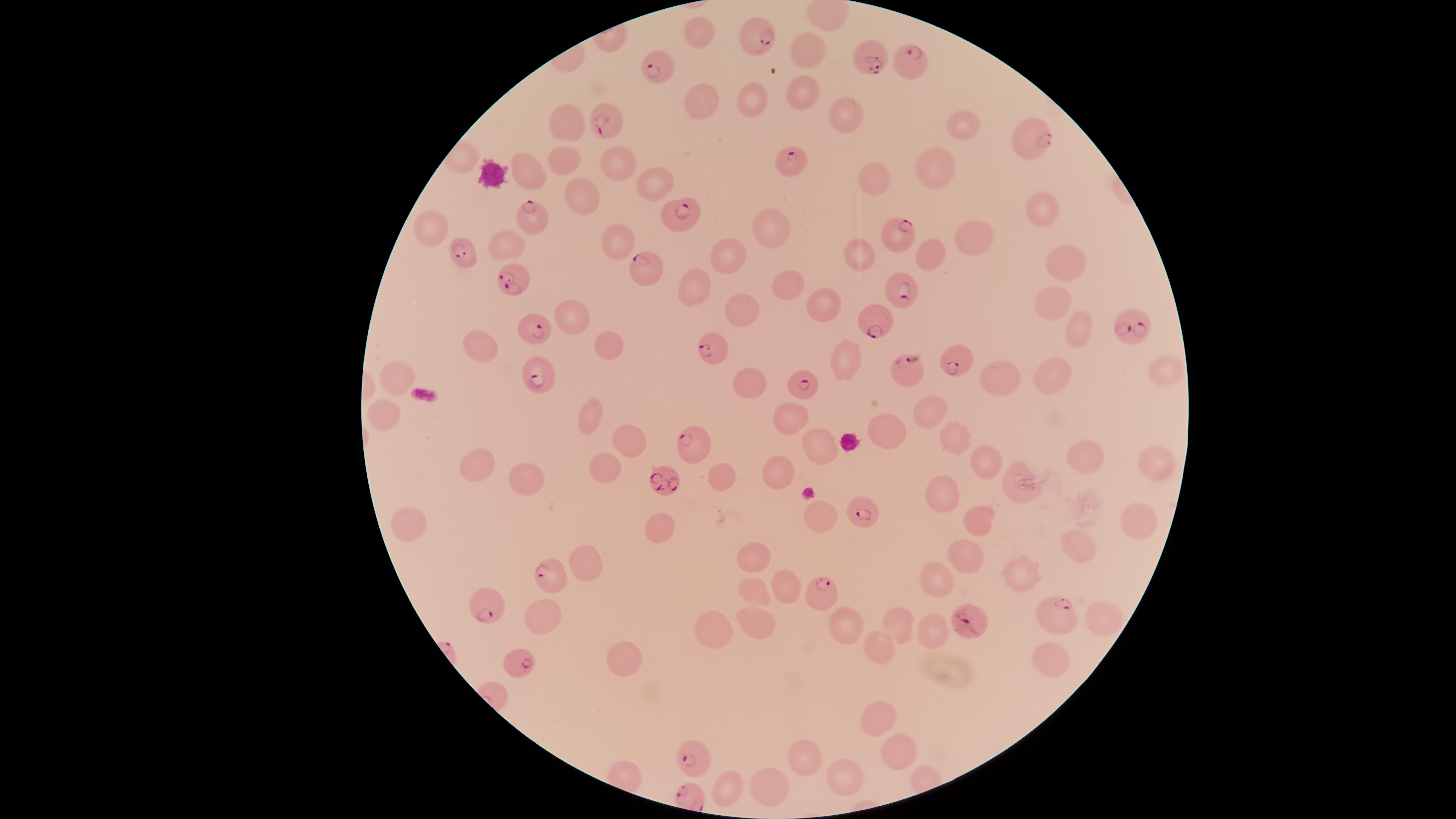

stain = Giemsa
image size = 1456×819 pixels
species = Plasmodium falciparum
capture = smartphone photograph through the microscope eyepiece
presence = malaria parasites detected
parasitized red blood cells = approximate marker points as (x, y) in pixels: (762, 39), (872, 60), (908, 61), (657, 63), (610, 121), (1033, 140), (790, 159), (684, 212), (529, 217), (894, 236), (461, 254), (649, 270), (511, 281), (903, 292), (878, 316), (536, 329), (1137, 329), (709, 350), (955, 360), (902, 366), (535, 377), (802, 381), (689, 437), (661, 486), (860, 511), (545, 573), (817, 593), (484, 605), (1064, 613), (968, 622), (520, 665), (693, 758)
preparation = thin blood smear
field of view = single
uninfected red blood cells = approximate marker points as (x, y) in pixels: (701, 33), (808, 52), (800, 96), (706, 98), (755, 100), (845, 118), (568, 121), (964, 125), (566, 162), (533, 165), (936, 166), (615, 168), (876, 178), (653, 183), (578, 197), (1040, 208), (772, 228), (433, 229), (977, 234), (506, 237), (618, 243), (934, 250), (864, 255), (727, 256), (1070, 262), (699, 283), (783, 283), (1054, 298), (825, 305), (744, 308), (573, 314), (1079, 324), (607, 345), (477, 349), (846, 358), (1156, 368), (1054, 372), (998, 376), (399, 378), (755, 378), (934, 408), (790, 411), (591, 413), (382, 415), (885, 422), (632, 436), (959, 438), (819, 446), (1086, 456), (984, 458), (480, 464), (1156, 465), (604, 473), (721, 473), (779, 473), (530, 481), (1026, 485), (941, 493), (410, 515), (820, 515), (1134, 519), (983, 523), (659, 526), (1077, 541), (753, 554), (966, 554), (591, 559), (1020, 568), (933, 576), (788, 582), (746, 590), (548, 612), (1101, 616), (755, 619), (712, 621), (846, 621), (903, 626), (933, 633), (880, 647), (627, 652), (1047, 656), (878, 716), (897, 745), (801, 757), (846, 777), (727, 786), (768, 786)
visible region = circular